Evaluate for parasitized red blood cells.
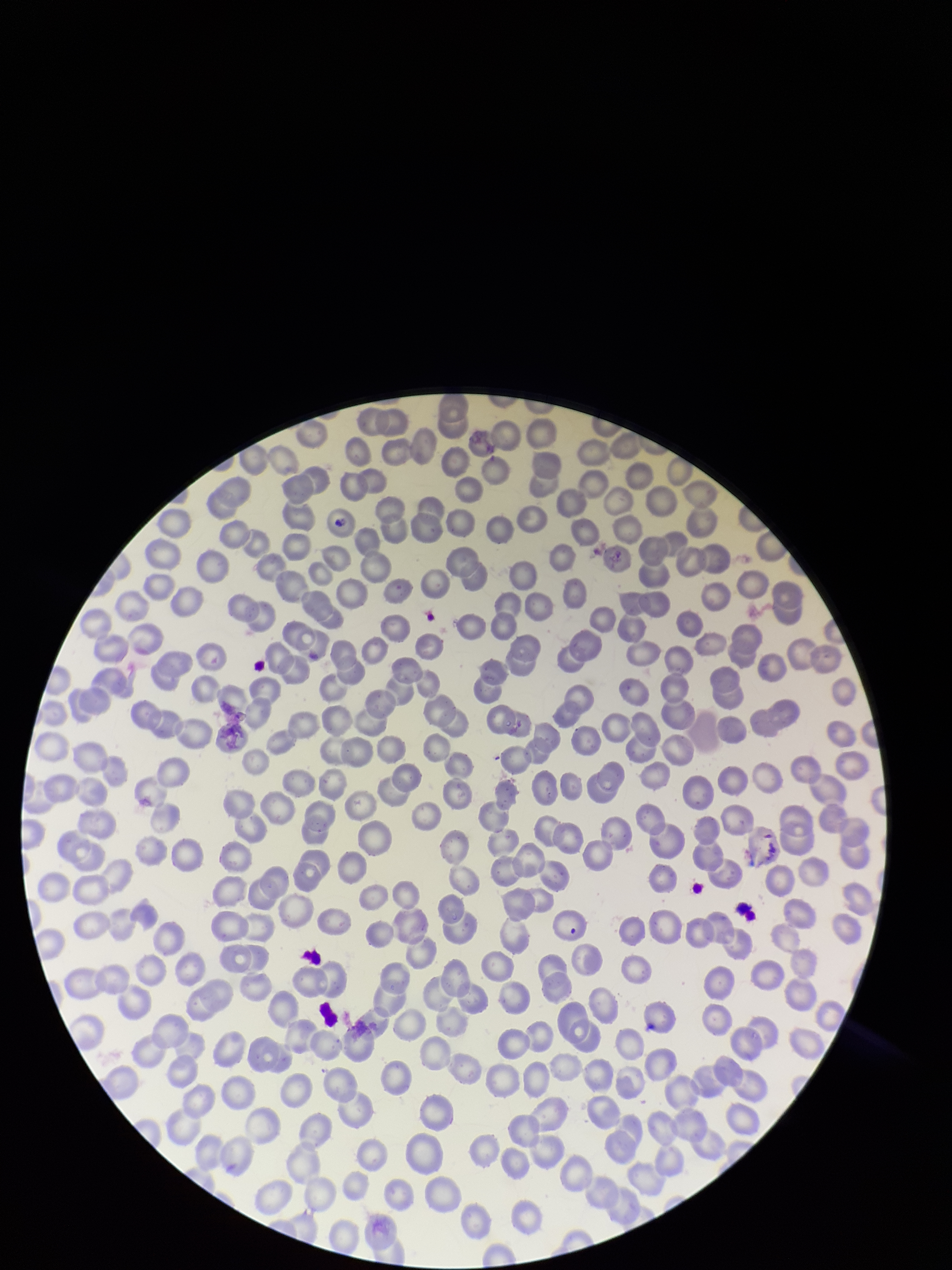
None seen.

Summary:
  - Preparation: thin
  - Patient malaria status: negative
  - Image size: 952×1270 pixels
  - Capture: smartphone photograph through the microscope eyepiece
  - Stain: Giemsa
  - Parasitized red blood cell count: 0
  - Red blood cell count: 271
  - Field of view: single